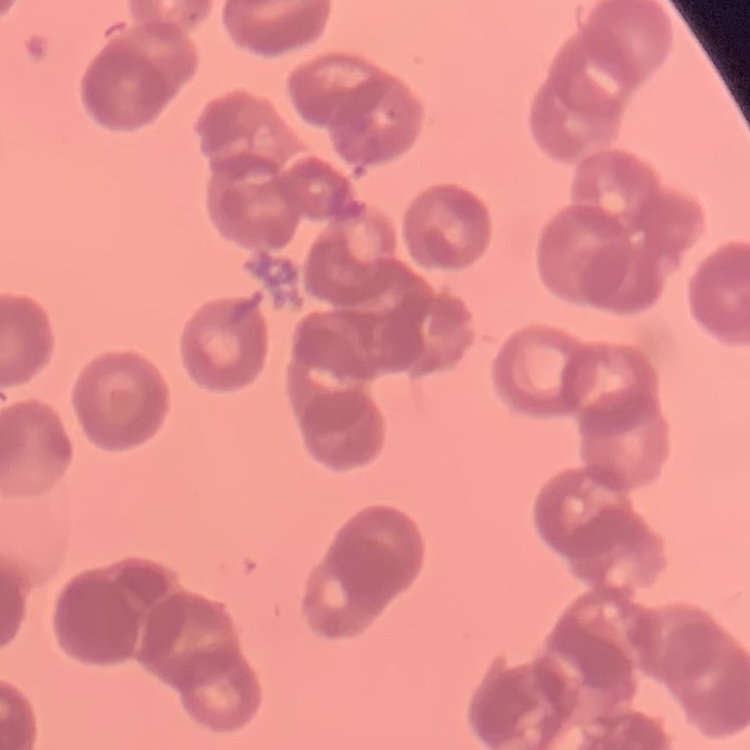
{
  "red_blood_cell_morphology": "rouleaux formation",
  "preparation": "thin blood film",
  "image_type": "one tile cut from a larger photomicrograph",
  "stain": "Field's or Giemsa"
}